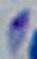

Summary:
  - Identification: Toxoplasma gondii
  - Modality: photomicrograph
  - Magnification: 1000x